Locate every leukocyte (white blood cell).
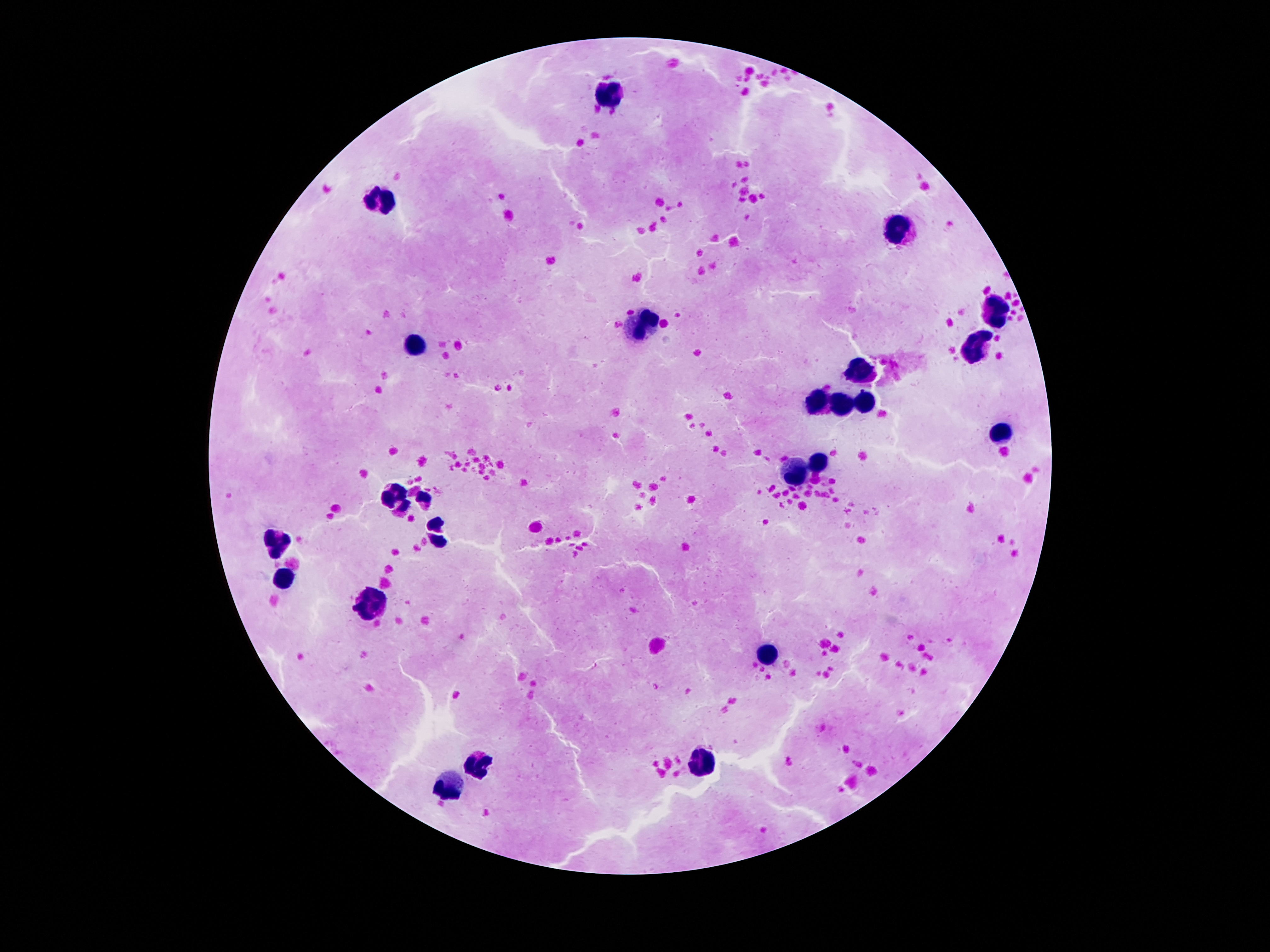
Approximate centers as {x, y} in pixels.
Leukocytes: {614, 93}, {381, 201}, {898, 230}, {994, 314}, {643, 326}, {414, 344}, {977, 348}, {858, 369}, {819, 398}, {866, 400}, {841, 405}, {1001, 433}, {819, 460}, {799, 475}, {391, 495}, {275, 544}, {287, 574}, {369, 604}, {769, 653}, {482, 762}, {703, 764}, {446, 789}.

Smartphone photograph taken through the microscope eyepiece. Image is 1270×952 pixels. 100x magnification. Thick blood film. Giemsa-stained preparation. Single field of view. Patient malaria status: uninfected.